Classify this cell by malaria status.
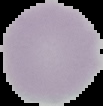
Uninfected.

From a thin blood film. Image is 103×106 pixels. Segmented cell region on a black background.